State the preparation type.
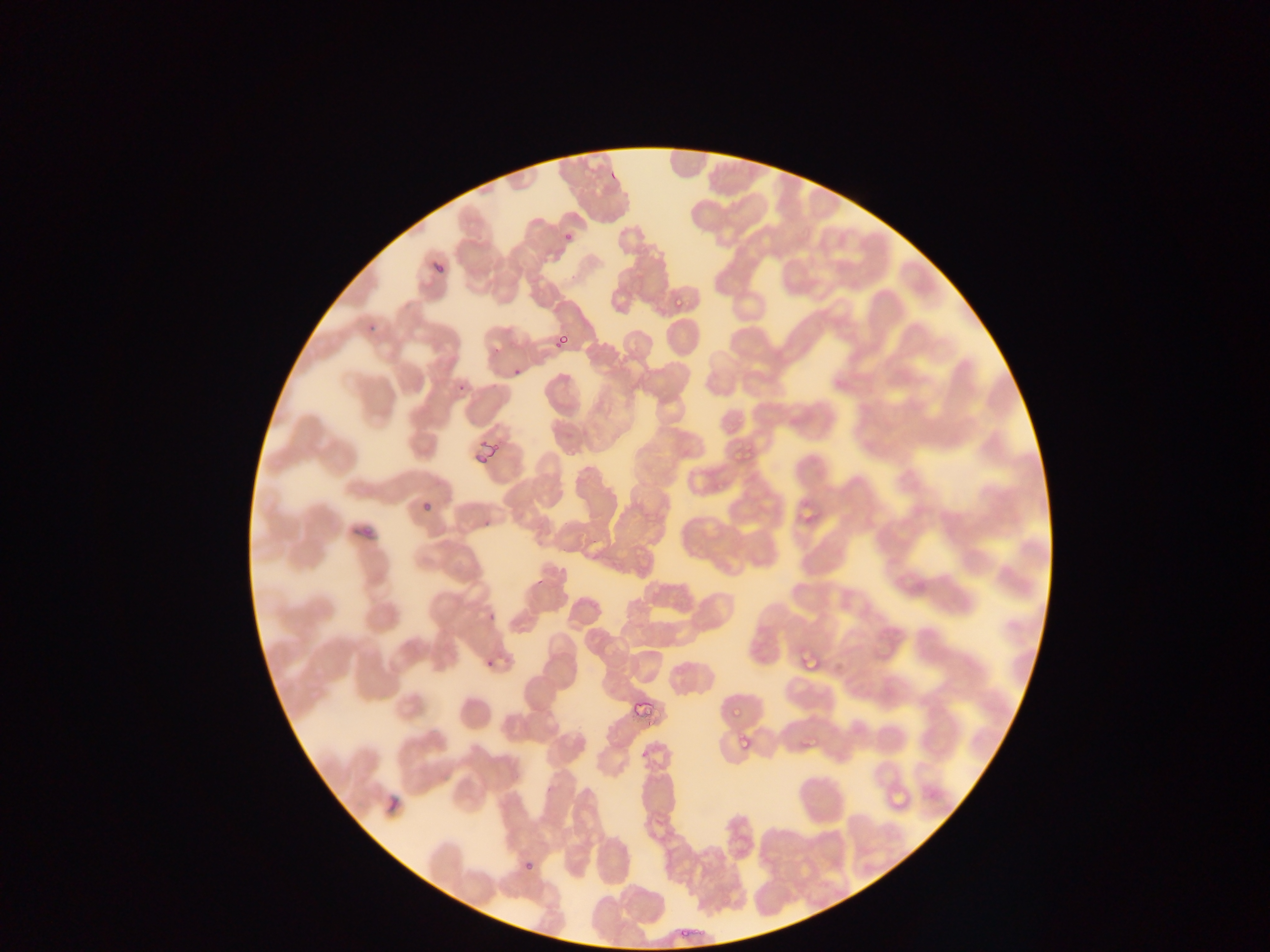
Thin blood smear.

Approximate bounding boxes as [left, top, right, bottom] in pixels. Leukocyte locations: [454, 691, 497, 738]. Malaria parasite locations (subset; some below the resolvable size): [562, 231, 576, 243], [431, 258, 450, 281], [674, 296, 686, 309], [557, 331, 575, 344], [553, 338, 561, 350], [510, 363, 526, 377], [458, 381, 465, 391], [730, 449, 739, 462], [743, 450, 756, 459], [481, 655, 493, 667], [730, 695, 747, 716], [739, 731, 755, 749], [523, 860, 541, 879]. Image is 1270×952 pixels. Mobile-phone photograph taken through the microscope. Single field of view. Collected in Ghana.